Locate every blood parasite and identify its species.
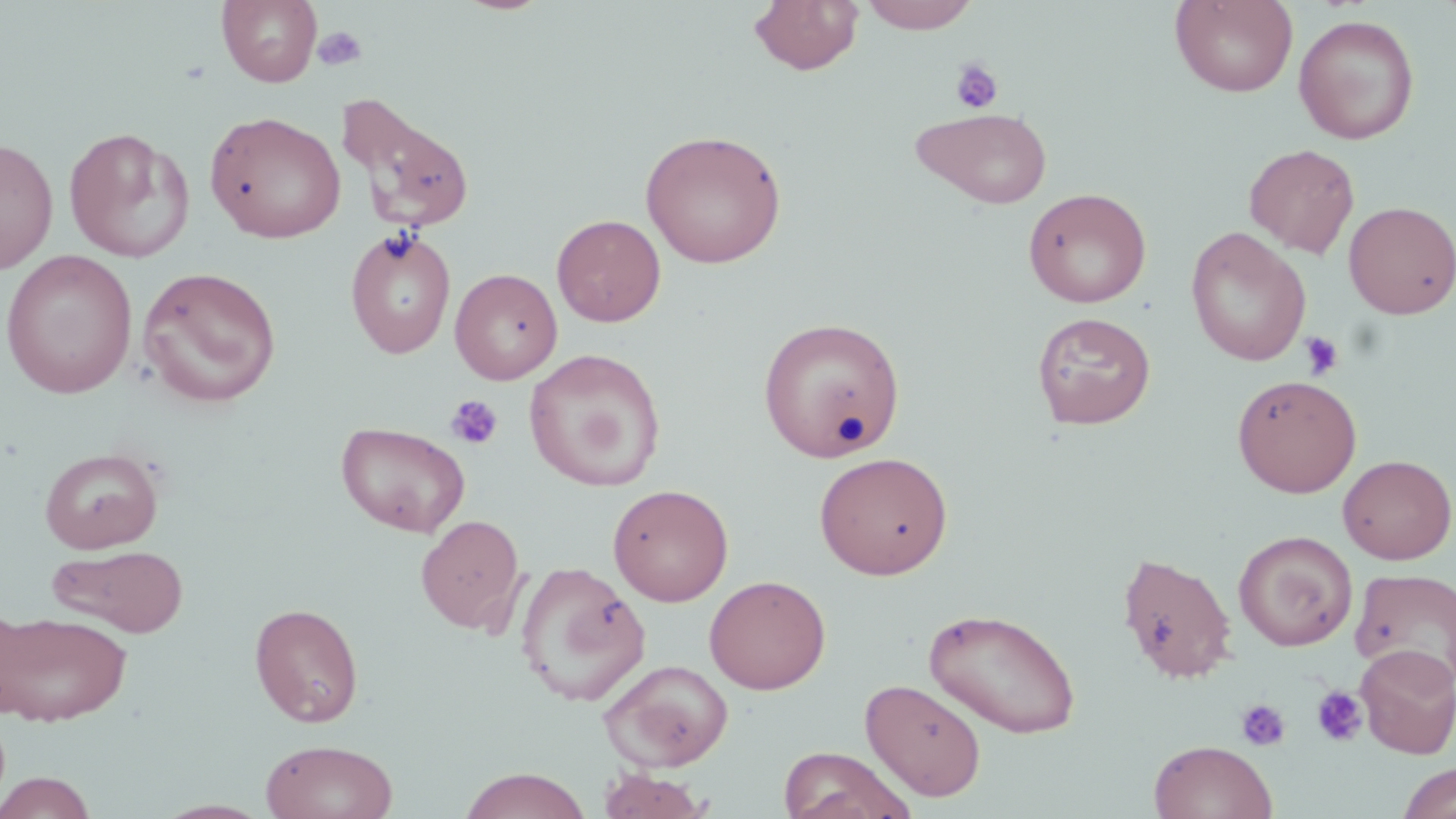

No blood parasites observed.

Summary:
  - Coordinate format: approximate bounding boxes as (x1, y1, x2, y2) in pixels
  - Platelet locations: (312, 26, 367, 71), (949, 57, 1005, 114), (1299, 330, 1345, 380), (444, 395, 503, 450), (1311, 685, 1368, 747), (1236, 698, 1291, 752)
  - Uninfected red blood cell locations: (217, 0, 322, 87), (748, 0, 864, 76), (858, 0, 981, 33), (1170, 1, 1298, 97), (1293, 14, 1420, 144), (344, 103, 475, 236), (910, 107, 1053, 208), (204, 111, 347, 244), (63, 127, 195, 264), (640, 129, 788, 268), (0, 137, 58, 275), (1244, 143, 1360, 258), (1023, 187, 1152, 308), (1343, 201, 1456, 319), (551, 214, 666, 327), (344, 227, 457, 360), (1185, 227, 1311, 367), (1, 249, 138, 399), (137, 266, 283, 408), (450, 268, 562, 384), (1032, 311, 1156, 429), (757, 316, 905, 462), (523, 347, 666, 492), (1232, 374, 1361, 497), (335, 421, 471, 538), (39, 447, 164, 554), (814, 451, 953, 579), (1337, 454, 1456, 564), (608, 483, 733, 606), (416, 515, 526, 634), (1233, 530, 1358, 651), (47, 544, 190, 637), (1116, 549, 1238, 684), (514, 560, 651, 707), (1350, 567, 1456, 687), (704, 574, 831, 694), (249, 603, 364, 727), (923, 606, 1082, 739), (0, 608, 133, 726), (1355, 644, 1456, 758), (599, 658, 734, 772), (860, 678, 987, 801), (260, 739, 399, 819), (1149, 740, 1277, 819), (777, 746, 916, 819), (1396, 762, 1456, 819), (458, 767, 593, 819), (597, 768, 712, 818), (0, 771, 99, 818), (153, 799, 273, 818)
  - Slide-level diagnosis: no evidence of blood parasites
  - Field of view: single
  - Modality: optical microscopy
  - Magnification: 1000x
  - Image size: 1456×819 pixels
  - Preparation: thin blood smear
  - Stain: May-Grünwald-Giemsa